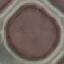

result = no malaria parasites detected
image type = cell patch, automatically extracted from a larger field of view and resized to 64 × 64 pixels
stain = Giemsa
capture = smartphone through the microscope eyepiece
preparation = thin smear